Comment on the morphology of the erythrocytes.
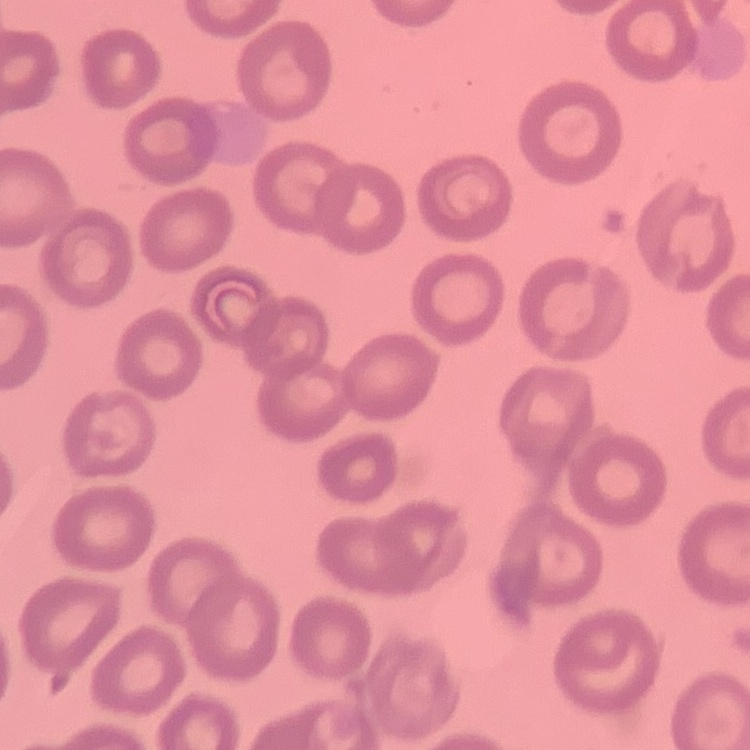
No rouleaux formation.

preparation = thin peripheral smear
image type = one tile cut from a larger photomicrograph
stain = Field's or Giemsa